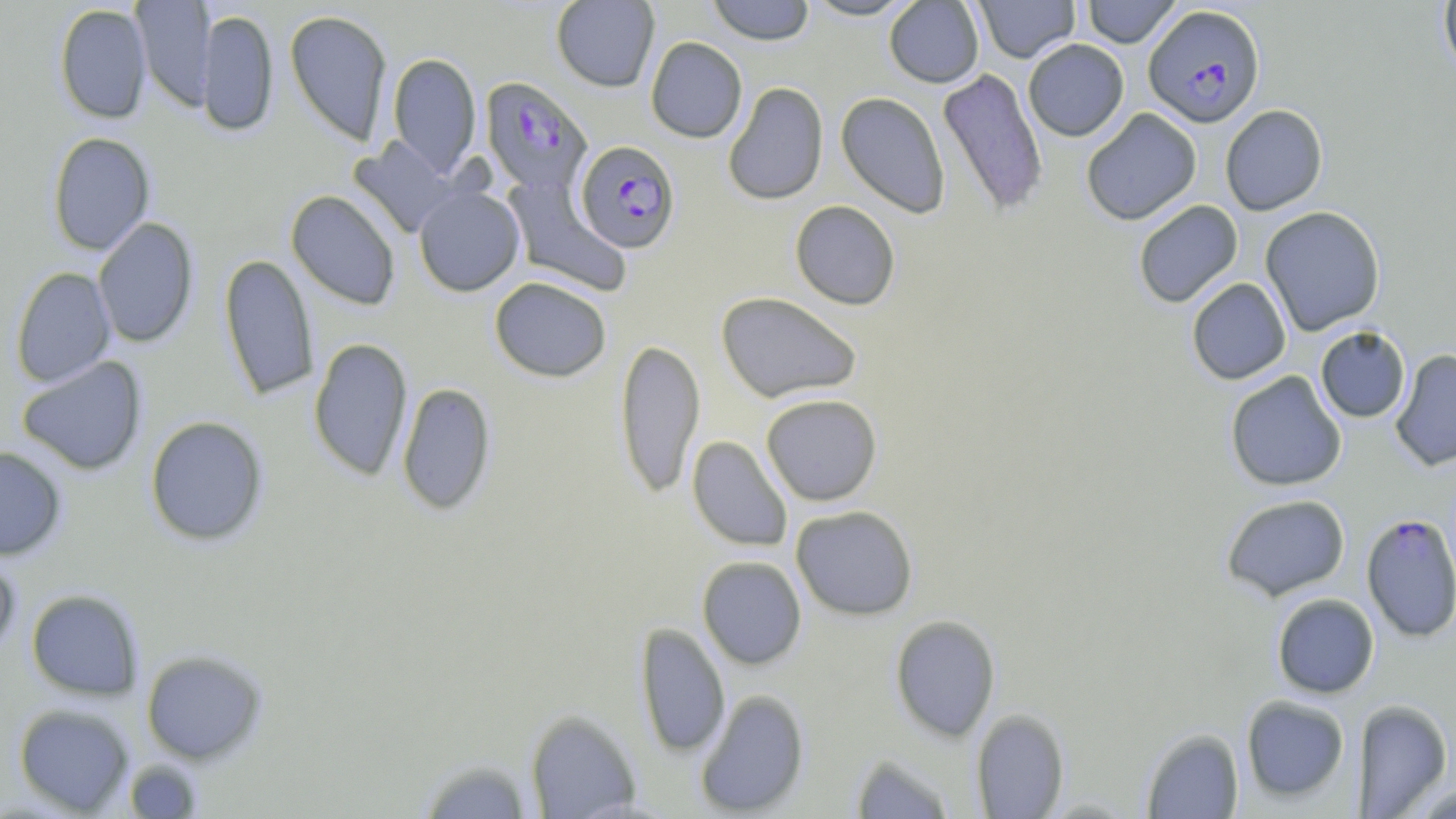
slide-level diagnosis = Plasmodium falciparum
uninfected red blood cell locations = approximate bounding boxes as named x1/y1/x2/y2 corners in pixels: (x1=131, y1=0, x2=215, y2=110), (x1=550, y1=0, x2=660, y2=92), (x1=706, y1=0, x2=816, y2=45), (x1=800, y1=0, x2=921, y2=21), (x1=883, y1=0, x2=984, y2=88), (x1=973, y1=0, x2=1080, y2=63), (x1=1080, y1=0, x2=1182, y2=48), (x1=1438, y1=0, x2=1456, y2=81), (x1=54, y1=3, x2=152, y2=125), (x1=197, y1=9, x2=278, y2=138), (x1=284, y1=10, x2=393, y2=146), (x1=645, y1=37, x2=747, y2=143), (x1=1023, y1=38, x2=1129, y2=141), (x1=387, y1=52, x2=482, y2=176), (x1=937, y1=68, x2=1049, y2=216), (x1=723, y1=81, x2=828, y2=206), (x1=836, y1=92, x2=950, y2=218), (x1=1220, y1=105, x2=1328, y2=216), (x1=1081, y1=108, x2=1202, y2=225), (x1=47, y1=132, x2=155, y2=255), (x1=349, y1=136, x2=462, y2=239), (x1=504, y1=177, x2=632, y2=296), (x1=413, y1=186, x2=526, y2=297), (x1=285, y1=190, x2=401, y2=310), (x1=1133, y1=200, x2=1243, y2=308), (x1=789, y1=201, x2=901, y2=310), (x1=1260, y1=205, x2=1385, y2=336), (x1=92, y1=217, x2=199, y2=348), (x1=218, y1=252, x2=319, y2=401), (x1=10, y1=267, x2=117, y2=388), (x1=489, y1=276, x2=612, y2=382), (x1=1186, y1=278, x2=1291, y2=385), (x1=715, y1=292, x2=863, y2=404), (x1=1315, y1=326, x2=1411, y2=424), (x1=308, y1=337, x2=414, y2=482), (x1=614, y1=338, x2=706, y2=499), (x1=1390, y1=349, x2=1456, y2=472), (x1=17, y1=356, x2=148, y2=476), (x1=1225, y1=370, x2=1347, y2=491), (x1=396, y1=381, x2=497, y2=516), (x1=760, y1=393, x2=883, y2=506), (x1=144, y1=415, x2=269, y2=546), (x1=687, y1=436, x2=793, y2=552), (x1=0, y1=446, x2=67, y2=561), (x1=1220, y1=494, x2=1351, y2=601), (x1=790, y1=505, x2=918, y2=621), (x1=0, y1=551, x2=20, y2=659), (x1=697, y1=556, x2=806, y2=670), (x1=26, y1=589, x2=145, y2=701), (x1=1271, y1=593, x2=1380, y2=699), (x1=889, y1=615, x2=1001, y2=742), (x1=635, y1=622, x2=730, y2=757), (x1=141, y1=649, x2=268, y2=765), (x1=694, y1=689, x2=810, y2=816), (x1=1240, y1=695, x2=1351, y2=802), (x1=1352, y1=699, x2=1453, y2=816), (x1=14, y1=703, x2=136, y2=816), (x1=525, y1=709, x2=642, y2=818), (x1=970, y1=709, x2=1069, y2=819), (x1=1140, y1=727, x2=1244, y2=818), (x1=850, y1=752, x2=958, y2=819), (x1=416, y1=756, x2=535, y2=819), (x1=122, y1=759, x2=205, y2=819), (x1=1408, y1=781, x2=1456, y2=818)
Plasmodium falciparum-infected red blood cell locations = approximate bounding boxes as named x1/y1/x2/y2 corners in pixels: (x1=1143, y1=4, x2=1265, y2=128), (x1=480, y1=76, x2=593, y2=195), (x1=575, y1=140, x2=680, y2=253), (x1=1361, y1=512, x2=1456, y2=642)
stain = May-Grünwald-Giemsa
image size = 1456×819 pixels
field of view = single
preparation = thin blood film
magnification = 1000x
modality = optical microscopy